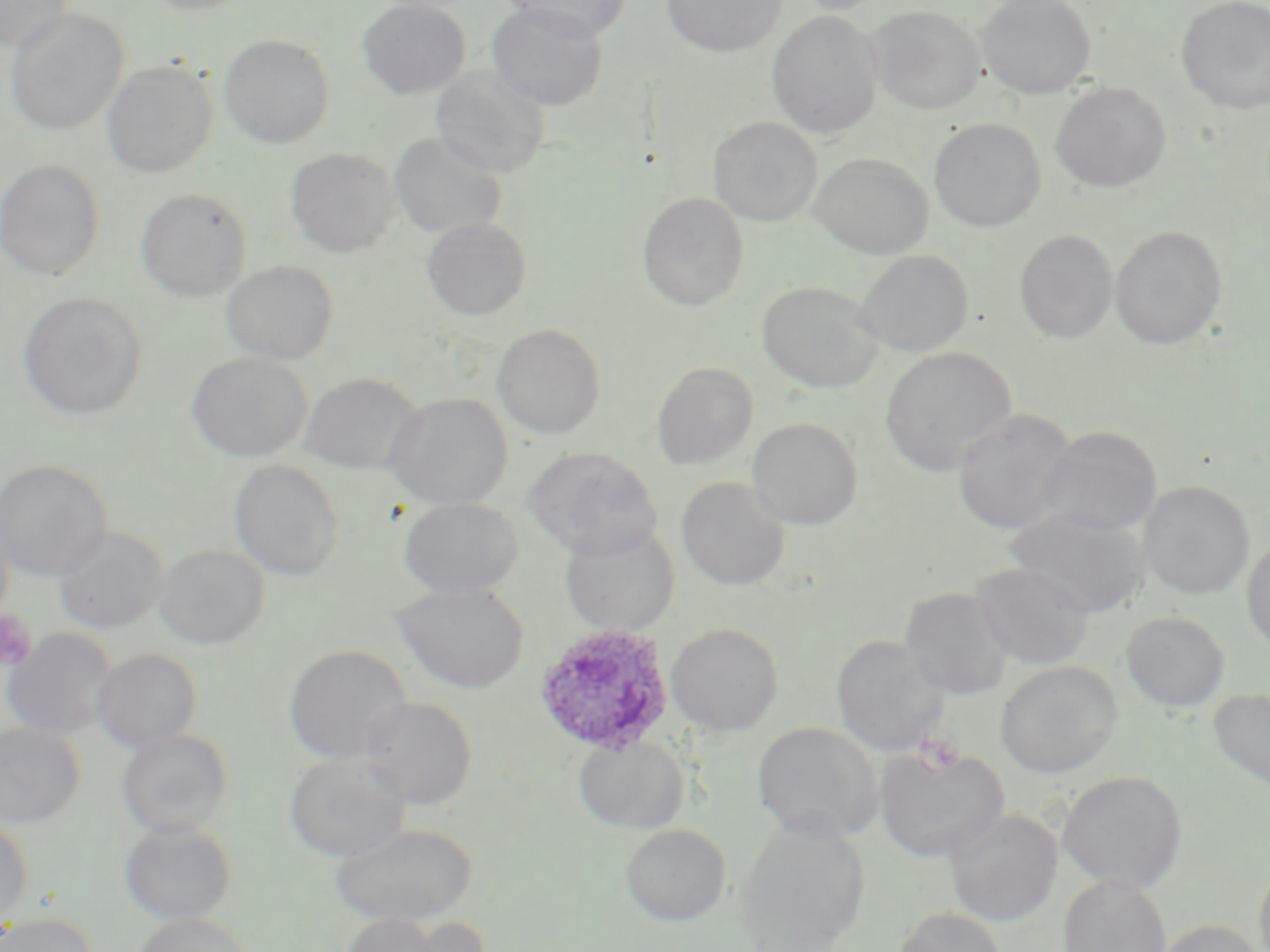
Approximate bounding boxes as (x1, y1, x2, y2) in pixels. Uninfected red blood cell locations: (139, 0, 256, 16), (357, 0, 471, 99), (506, 0, 633, 39), (661, 0, 787, 57), (788, 0, 891, 16), (975, 0, 1096, 100), (0, 1, 74, 52), (1176, 1, 1270, 113), (487, 3, 609, 111), (866, 5, 986, 115), (4, 8, 129, 135), (766, 11, 884, 138), (219, 34, 335, 148), (101, 60, 218, 179), (430, 68, 550, 179), (1050, 82, 1172, 193), (708, 116, 822, 226), (928, 118, 1046, 232), (389, 132, 508, 239), (285, 147, 400, 258), (808, 154, 934, 259), (0, 158, 106, 281), (135, 187, 252, 302), (637, 192, 749, 311), (422, 216, 532, 321), (1110, 225, 1228, 350), (1014, 229, 1119, 344), (854, 249, 974, 356), (221, 260, 339, 365), (757, 280, 884, 393), (17, 291, 148, 420), (492, 323, 606, 439), (880, 346, 1017, 476), (186, 353, 311, 463), (651, 362, 759, 471), (298, 372, 424, 474), (383, 392, 513, 510), (952, 408, 1077, 535), (746, 417, 863, 530), (1036, 424, 1163, 537), (523, 447, 663, 559), (0, 459, 112, 582), (228, 459, 345, 582), (676, 477, 791, 591), (1138, 481, 1256, 600), (399, 497, 524, 599), (1003, 508, 1148, 618), (0, 509, 14, 626), (559, 523, 680, 637), (52, 526, 168, 635), (1241, 533, 1270, 653), (154, 544, 270, 649), (971, 562, 1096, 669), (391, 582, 530, 694), (900, 587, 1014, 700), (1120, 612, 1230, 712), (666, 622, 784, 736), (2, 629, 118, 739), (831, 634, 950, 756), (283, 644, 412, 765), (92, 648, 203, 754), (996, 660, 1122, 779), (1209, 688, 1270, 790), (359, 696, 478, 810), (751, 722, 883, 844), (0, 724, 85, 828), (115, 728, 234, 840), (573, 734, 689, 834), (873, 744, 1009, 863), (284, 752, 410, 863), (1056, 771, 1188, 893), (944, 808, 1063, 926), (0, 815, 34, 930), (733, 816, 871, 952), (119, 821, 237, 925), (330, 823, 477, 926), (620, 823, 731, 926), (1254, 863, 1270, 952), (1058, 874, 1173, 952), (891, 907, 1007, 952), (0, 913, 98, 952), (131, 914, 252, 952), (336, 914, 453, 952), (388, 917, 496, 952), (1154, 919, 1265, 952). Platelet locations: (0, 610, 37, 670), (915, 731, 966, 774). Plasmodium ovale-infected red blood cell locations: (533, 623, 676, 758). Slide-level diagnosis: Plasmodium ovale. May-Grünwald-Giemsa-stained preparation. Optical microscopy. Thin blood smear. Captured at 1000x magnification. One field of a larger specimen. Image is 1270×952 pixels.